Assess the morphology of the erythrocytes.
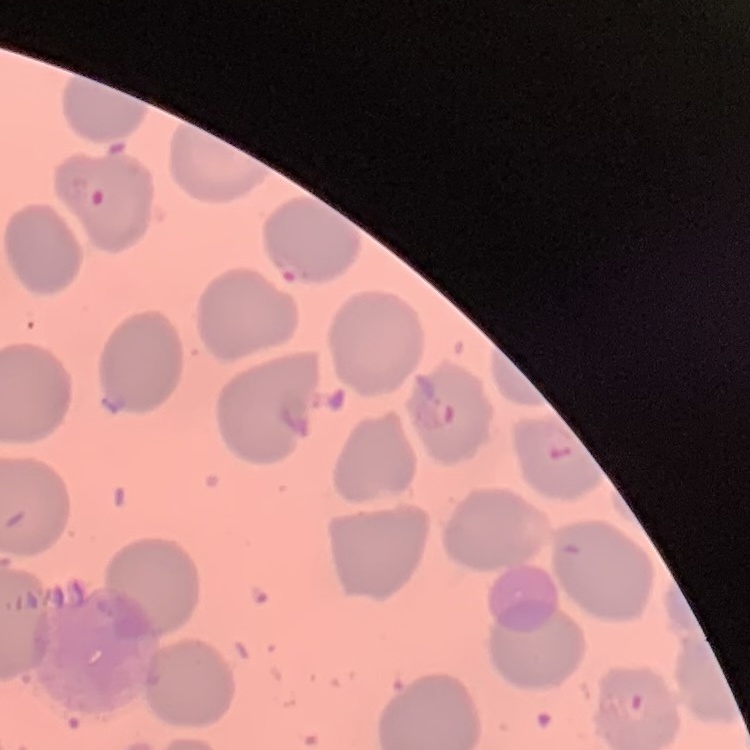
No rouleaux formation.

One tile cut from a larger photomicrograph. Thin blood film. Stained with either Field's or Giemsa.